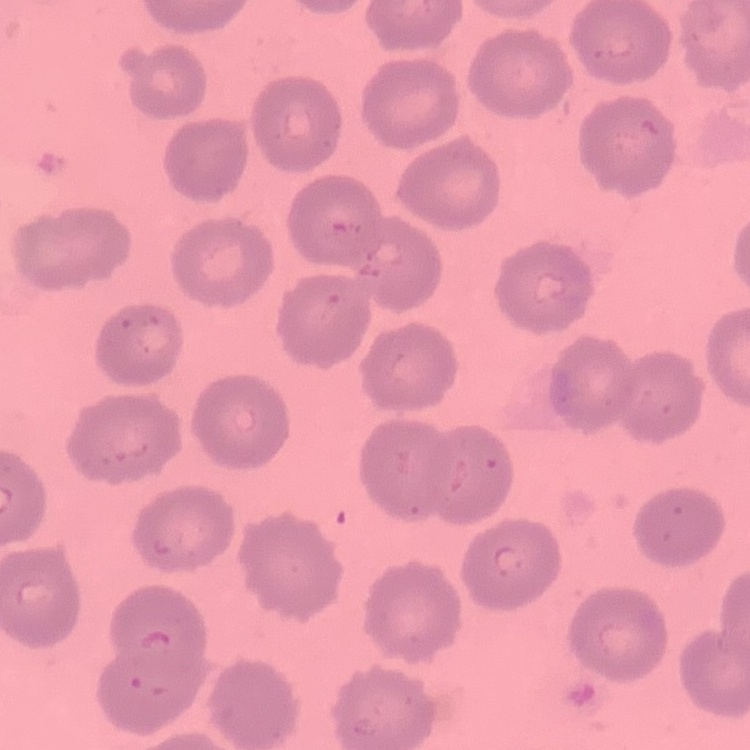

Summary:
  - Erythrocyte morphology: no rouleaux formation
  - Stain: Field's or Giemsa
  - Preparation: thin blood film
  - Image type: one tile cut from a larger photomicrograph